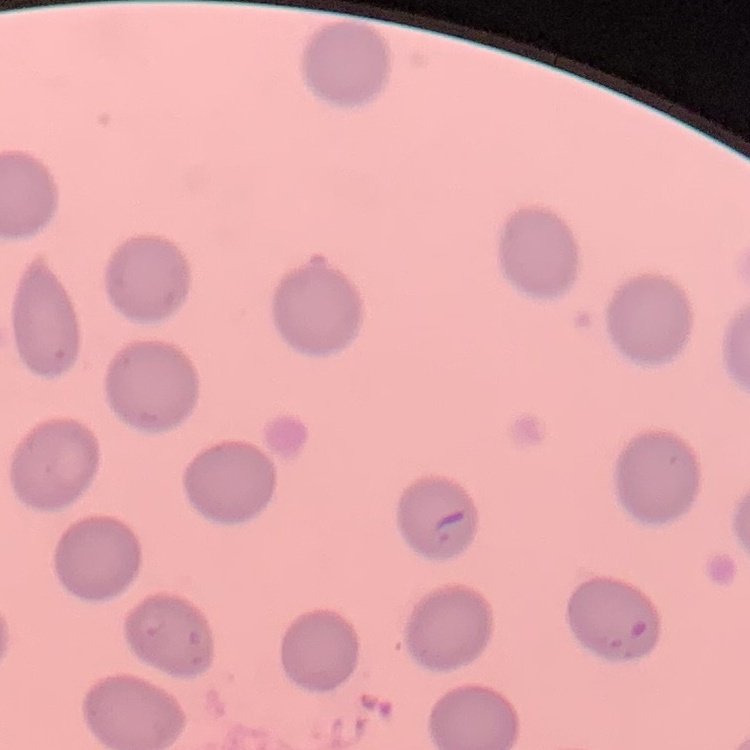
Summary:
  - Erythrocyte morphology: no rouleaux formation
  - Image type: square crop of a larger photomicrograph
  - Stain: Field's or Giemsa
  - Preparation: thin peripheral smear